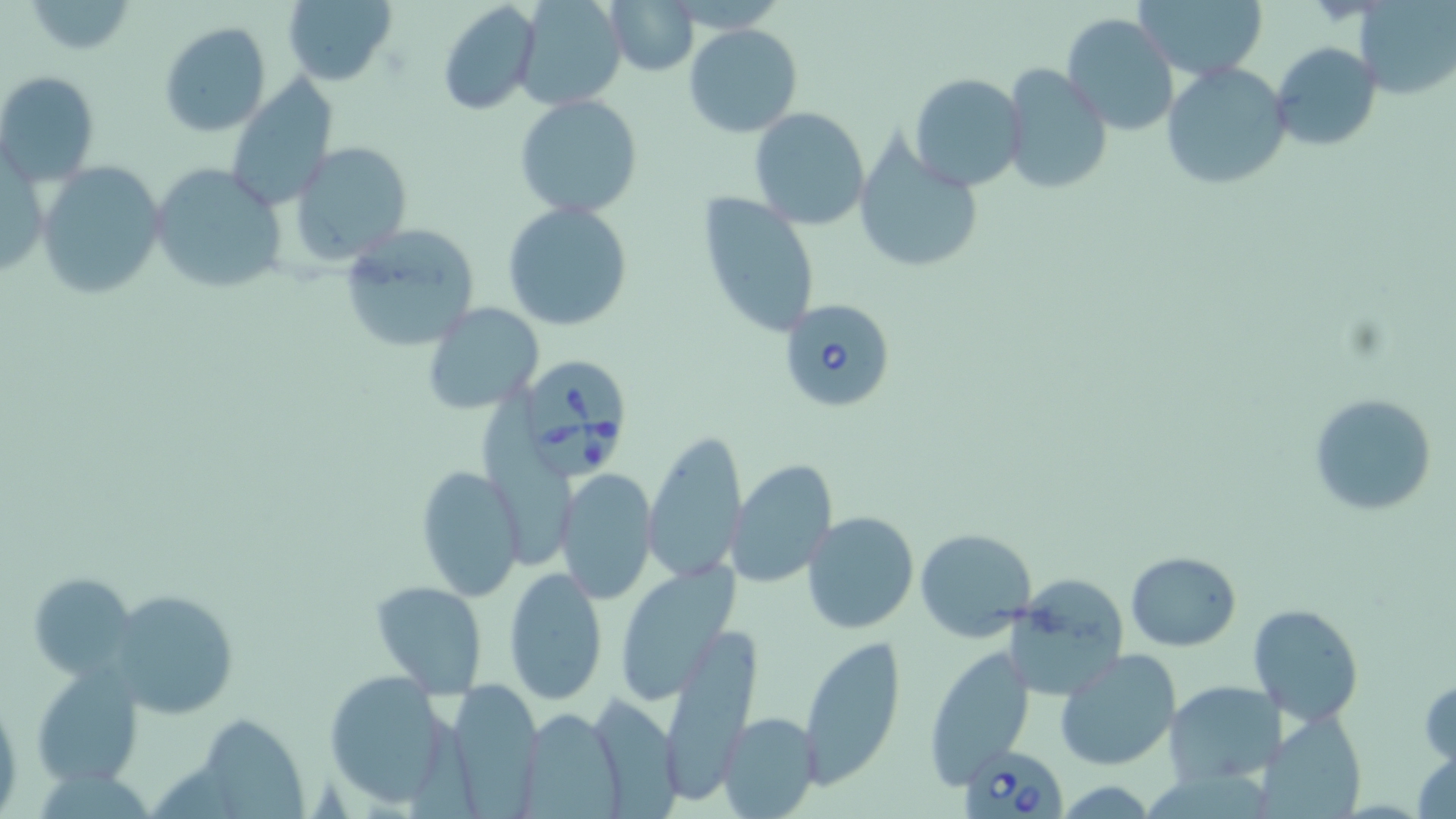 Approximate bounding boxes as [x1, y1, x2, y2] in pixels. Uninfected red blood cell locations: [282, 0, 398, 88], [514, 0, 626, 112], [605, 0, 700, 75], [1136, 0, 1269, 81], [1355, 0, 1455, 99], [22, 1, 137, 55], [437, 1, 541, 117], [1062, 13, 1180, 136], [157, 22, 272, 137], [684, 24, 803, 137], [1271, 41, 1381, 152], [1162, 62, 1292, 193], [999, 66, 1113, 197], [0, 70, 101, 187], [909, 73, 1028, 192], [223, 76, 338, 212], [515, 94, 642, 220], [750, 108, 870, 229], [853, 137, 987, 276], [293, 142, 412, 264], [36, 161, 166, 300], [150, 163, 289, 294], [696, 190, 820, 340], [503, 201, 633, 331], [340, 225, 479, 355], [423, 301, 545, 415], [482, 386, 574, 562], [1308, 393, 1436, 515], [642, 432, 749, 584], [728, 458, 838, 587], [414, 466, 526, 602], [556, 468, 657, 605], [802, 512, 920, 633], [914, 527, 1036, 641], [1126, 552, 1242, 651], [614, 564, 737, 701], [504, 566, 607, 705], [29, 573, 138, 680], [370, 580, 488, 697], [1007, 580, 1130, 701], [107, 590, 237, 717], [1249, 604, 1364, 726], [667, 625, 766, 797], [796, 636, 907, 786], [921, 647, 1035, 789], [1055, 650, 1180, 770], [31, 666, 143, 786], [322, 668, 454, 811], [1419, 674, 1455, 766], [444, 679, 543, 813], [1163, 681, 1284, 786], [593, 690, 687, 819], [0, 691, 22, 819], [514, 706, 629, 817], [719, 710, 820, 819], [1256, 711, 1368, 819], [192, 715, 306, 817], [1413, 749, 1456, 819], [1053, 779, 1160, 815]. Babesia divergens-infected red blood cell locations: [777, 295, 900, 416], [510, 355, 634, 484], [960, 744, 1068, 818]. Slide-level diagnosis: Babesia divergens. Optical microscopy. May-Grünwald-Giemsa-stained preparation. 1000x magnification. Thin blood smear. Single field of view. Image is 1456×819 pixels.